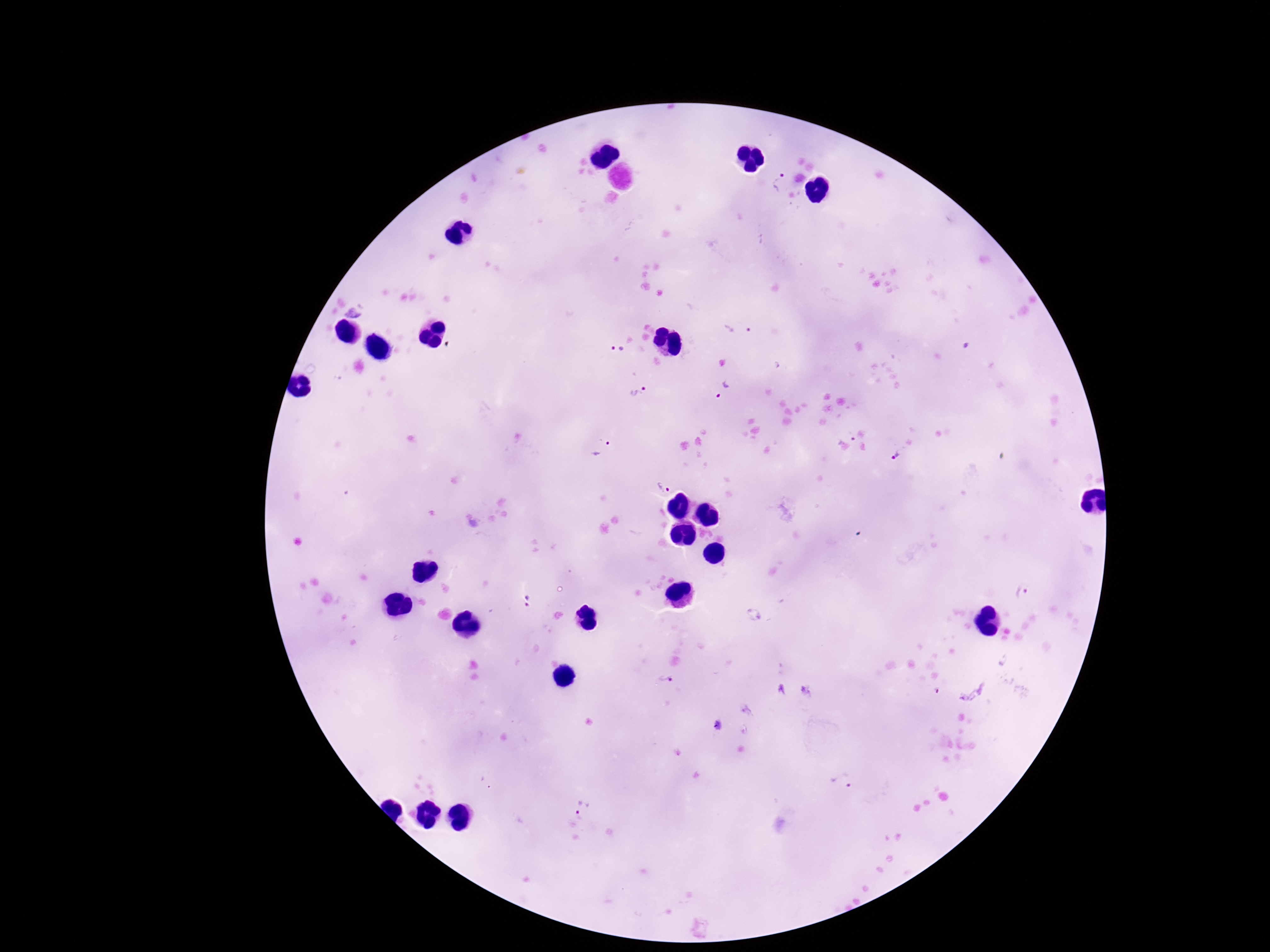

Approximate centers as [x, y] in pixels.
Summary:
  - Plasmodium parasite locations: [780, 184], [354, 311], [739, 328], [618, 348], [639, 392], [723, 392], [850, 434], [603, 446], [895, 455], [664, 487], [1021, 593], [666, 677], [845, 784], [582, 809]
  - Magnification: 100x
  - Capture: smartphone camera through the microscope eyepiece
  - Patient malaria status: positive
  - Field of view: single
  - Stain: Giemsa
  - Image size: 1270×952 pixels
  - Preparation: thick peripheral-blood smear